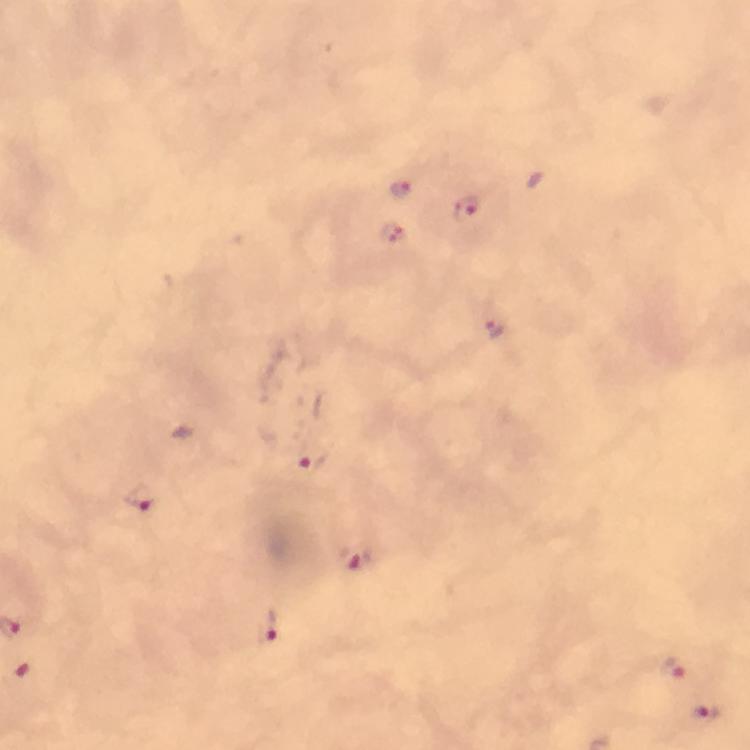

Approximate centers as (x, y) in pixels. Malaria parasite locations: (400, 189), (468, 209), (393, 236), (493, 327), (308, 459), (137, 497), (357, 559), (266, 626), (673, 667), (705, 712). Photographed through the microscope with a smartphone camera. At 100x magnification. Thick blood film. From a malaria diagnostic workup. Immersion oil was used. Cropped region of a single field of view. Giemsa stain. Image is 750×750 pixels.